Locate and identify every blood parasite.
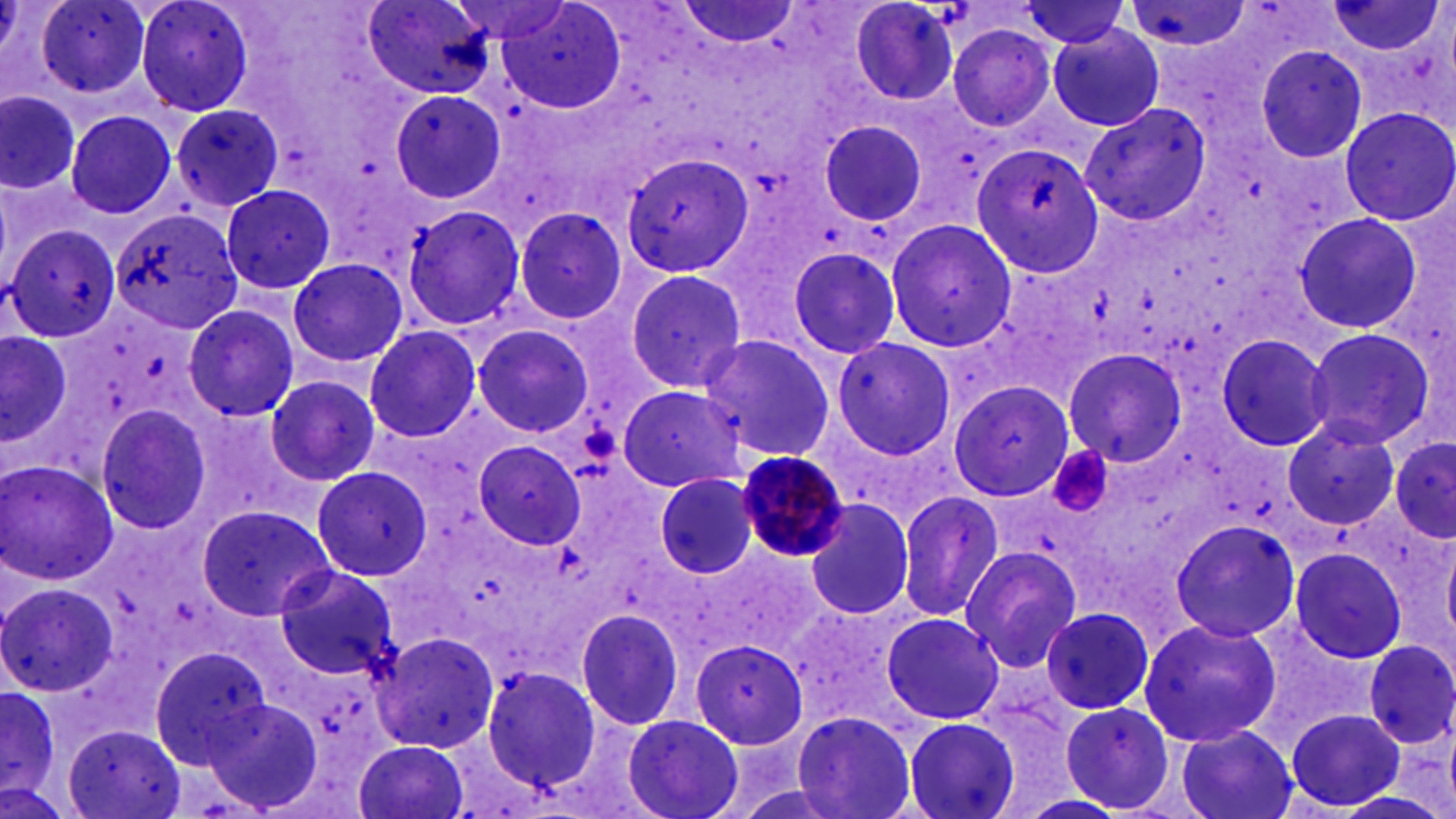
Approximate bounding boxes as named x1/y1/x2/y2 corners in pixels.
Plasmodium malariae-infected red blood cells: (x1=734, y1=449, x2=847, y2=563).
No Plasmodium falciparum, Plasmodium ovale, Plasmodium vivax, Babesia divergens, or Trypanosoma brucei observed.

slide-level diagnosis = Plasmodium malariae
magnification = 1000x
platelet locations = approximate bounding boxes as named x1/y1/x2/y2 corners in pixels: (x1=1056, y1=448, x2=1116, y2=519)
modality = light microscopy
uninfected red blood cell locations = approximate bounding boxes as named x1/y1/x2/y2 corners in pixels: (x1=36, y1=0, x2=154, y2=97), (x1=133, y1=0, x2=257, y2=118), (x1=362, y1=0, x2=495, y2=98), (x1=1014, y1=0, x2=1134, y2=49), (x1=1327, y1=0, x2=1445, y2=58), (x1=1123, y1=1, x2=1252, y2=56), (x1=677, y1=2, x2=802, y2=48), (x1=845, y1=2, x2=960, y2=107), (x1=488, y1=3, x2=628, y2=113), (x1=1046, y1=22, x2=1166, y2=132), (x1=946, y1=24, x2=1057, y2=132), (x1=1254, y1=45, x2=1369, y2=165), (x1=387, y1=87, x2=508, y2=205), (x1=1, y1=89, x2=83, y2=196), (x1=170, y1=103, x2=284, y2=211), (x1=1080, y1=104, x2=1210, y2=226), (x1=1338, y1=107, x2=1456, y2=226), (x1=67, y1=111, x2=178, y2=220), (x1=819, y1=118, x2=930, y2=230), (x1=971, y1=141, x2=1103, y2=279), (x1=620, y1=150, x2=754, y2=278), (x1=220, y1=183, x2=337, y2=296), (x1=400, y1=203, x2=524, y2=331), (x1=513, y1=207, x2=627, y2=325), (x1=112, y1=208, x2=243, y2=335), (x1=1295, y1=212, x2=1423, y2=334), (x1=885, y1=217, x2=1018, y2=353), (x1=6, y1=223, x2=121, y2=343), (x1=786, y1=243, x2=905, y2=359), (x1=288, y1=258, x2=408, y2=369), (x1=621, y1=266, x2=748, y2=394), (x1=181, y1=303, x2=300, y2=423), (x1=473, y1=324, x2=594, y2=438), (x1=363, y1=325, x2=482, y2=444), (x1=1303, y1=325, x2=1437, y2=452), (x1=1, y1=328, x2=75, y2=450), (x1=697, y1=332, x2=837, y2=461), (x1=1215, y1=333, x2=1335, y2=453), (x1=829, y1=335, x2=957, y2=460), (x1=1061, y1=348, x2=1188, y2=465), (x1=264, y1=374, x2=380, y2=486), (x1=947, y1=379, x2=1075, y2=501), (x1=616, y1=384, x2=749, y2=493), (x1=93, y1=403, x2=216, y2=536), (x1=1282, y1=422, x2=1399, y2=530), (x1=1388, y1=435, x2=1454, y2=545), (x1=471, y1=440, x2=586, y2=550), (x1=0, y1=461, x2=119, y2=585), (x1=312, y1=466, x2=433, y2=581), (x1=651, y1=471, x2=761, y2=581), (x1=894, y1=484, x2=1005, y2=619), (x1=805, y1=499, x2=915, y2=621), (x1=196, y1=506, x2=335, y2=621), (x1=1168, y1=517, x2=1302, y2=643), (x1=959, y1=543, x2=1086, y2=672), (x1=1288, y1=547, x2=1409, y2=664), (x1=270, y1=564, x2=400, y2=682), (x1=1, y1=579, x2=118, y2=697), (x1=1041, y1=605, x2=1156, y2=716), (x1=578, y1=609, x2=687, y2=731), (x1=879, y1=611, x2=1007, y2=727), (x1=1136, y1=617, x2=1283, y2=748), (x1=373, y1=631, x2=500, y2=753), (x1=689, y1=638, x2=808, y2=750), (x1=1361, y1=640, x2=1456, y2=751), (x1=149, y1=645, x2=270, y2=766), (x1=482, y1=665, x2=603, y2=792), (x1=0, y1=681, x2=64, y2=805), (x1=201, y1=693, x2=324, y2=816), (x1=1058, y1=702, x2=1174, y2=813), (x1=792, y1=706, x2=922, y2=819), (x1=1286, y1=708, x2=1405, y2=813), (x1=621, y1=713, x2=743, y2=819), (x1=901, y1=716, x2=1023, y2=819), (x1=61, y1=724, x2=186, y2=818), (x1=1174, y1=725, x2=1300, y2=819), (x1=357, y1=740, x2=469, y2=817), (x1=1012, y1=793, x2=1129, y2=819)
preparation = thin blood smear
field of view = single
stain = May-Grünwald-Giemsa
image size = 1456×819 pixels